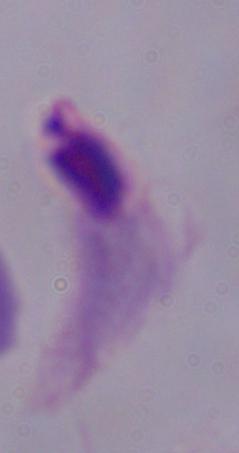

modality = photomicrograph
identification = trichomonad
magnification = 1000x